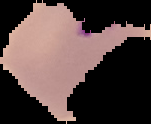
Image is 151×124 pixels. Malaria status: parasitized. From a thin blood film. The area outside the segmented cell region is set to black.